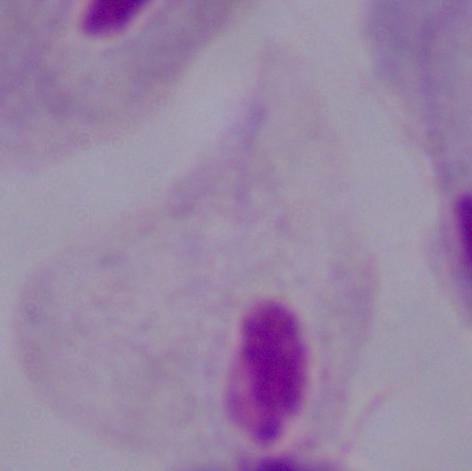

Summary:
  - Magnification: 1000x
  - Identification: trichomonad
  - Modality: micrograph